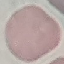

Result: no malaria parasites seen. Acquired by smartphone through the microscope eyepiece. Automatically extracted cell patch, resized to 64 × 64 pixels. Thin blood smear. Giemsa-stained preparation.